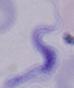

Summary:
  - Identification: trypanosome
  - Magnification: 1000x
  - Modality: micrograph